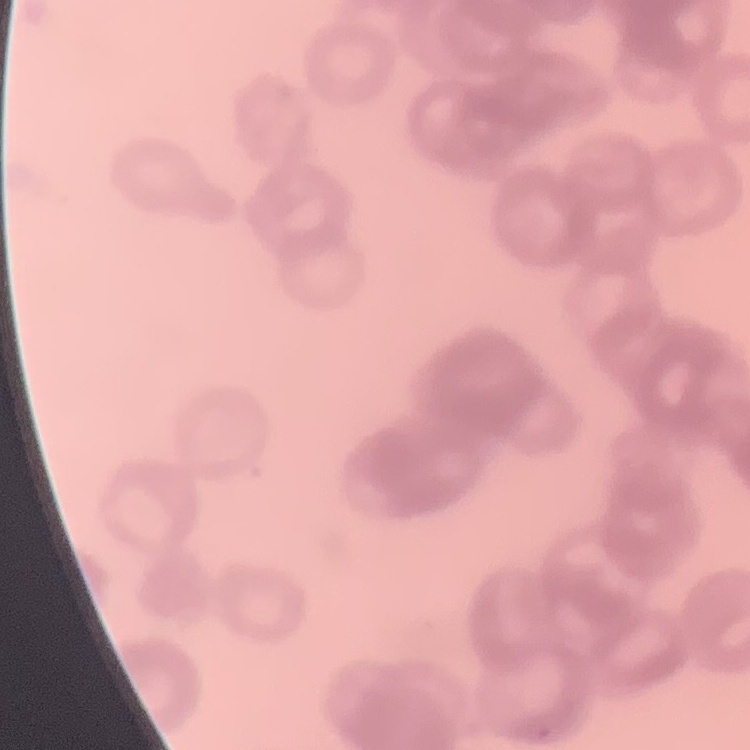
Summary:
  - Erythrocyte morphology: rouleaux formation
  - Preparation: thin blood smear
  - Stain: Field's or Giemsa
  - Image type: one tile cut from a larger photomicrograph